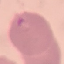
malaria status = parasitized
stain = Giemsa
preparation = thin blood smear
capture = smartphone camera at the microscope eyepiece
image type = automatically extracted cell patch, resized to 64 × 64 pixels